Name the parasite shown.
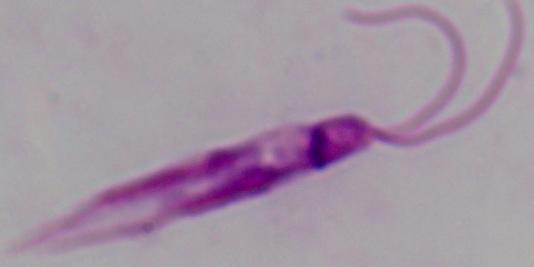
Leishmania.

1000x magnification. Photomicrograph.